Point out each Plasmodium parasite.
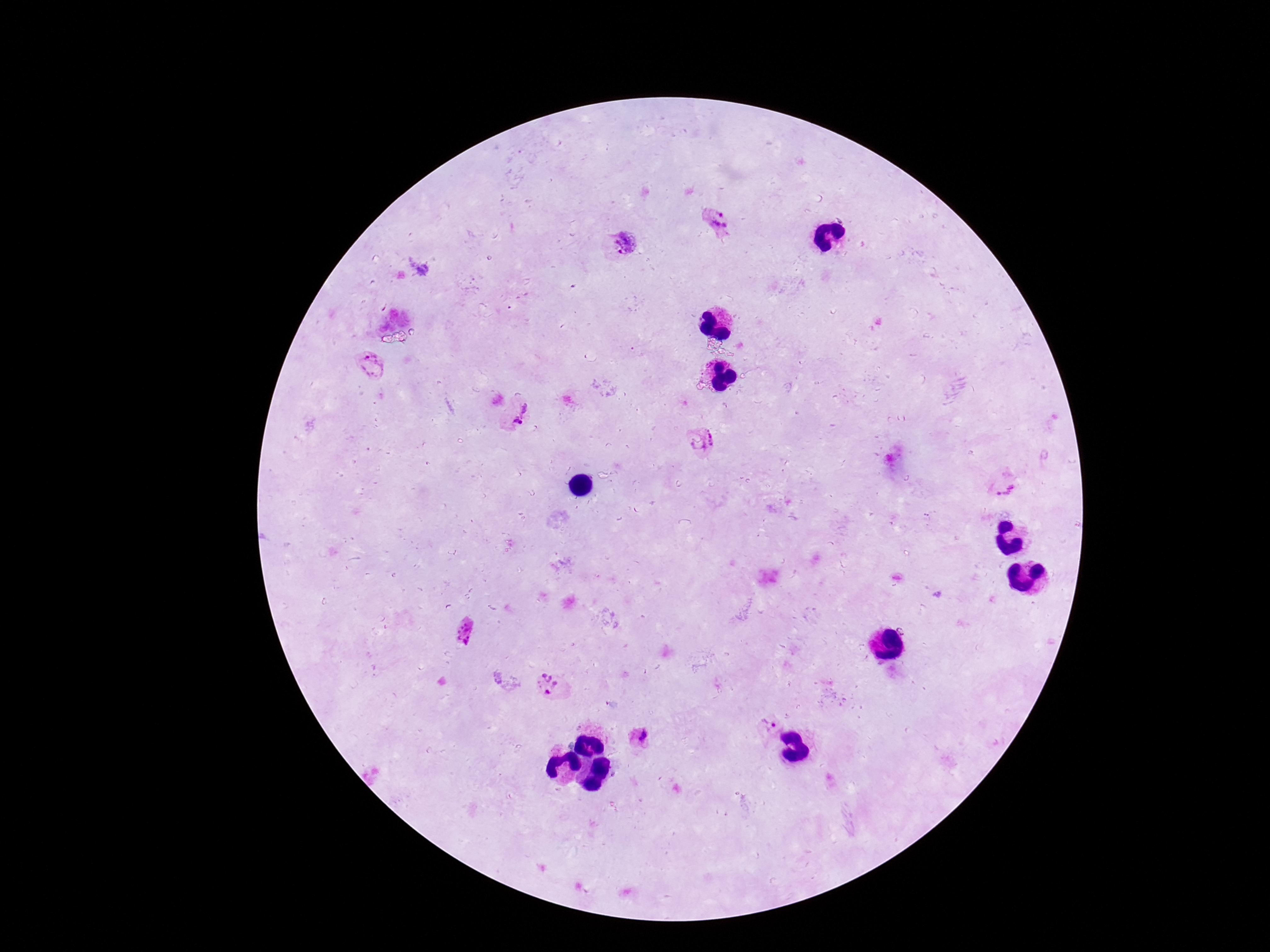

Approximate centers as [x, y] in pixels.
Plasmodium parasites: [717, 222], [626, 243], [370, 365], [519, 413], [703, 438], [1005, 485], [466, 630], [548, 684], [770, 723], [641, 738].

Summary:
  - Stain: Giemsa
  - Preparation: thick blood film
  - Magnification: 100x
  - Patient malaria status: infected
  - Capture: smartphone camera through the microscope eyepiece
  - Field of view: single
  - Image size: 1270×952 pixels